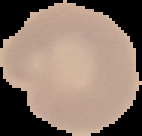
Result: no malaria parasites detected. Segmented cell region on a black background. Image is 142×136 pixels. From a thin blood film.